Locate every blood parasite and identify its species.
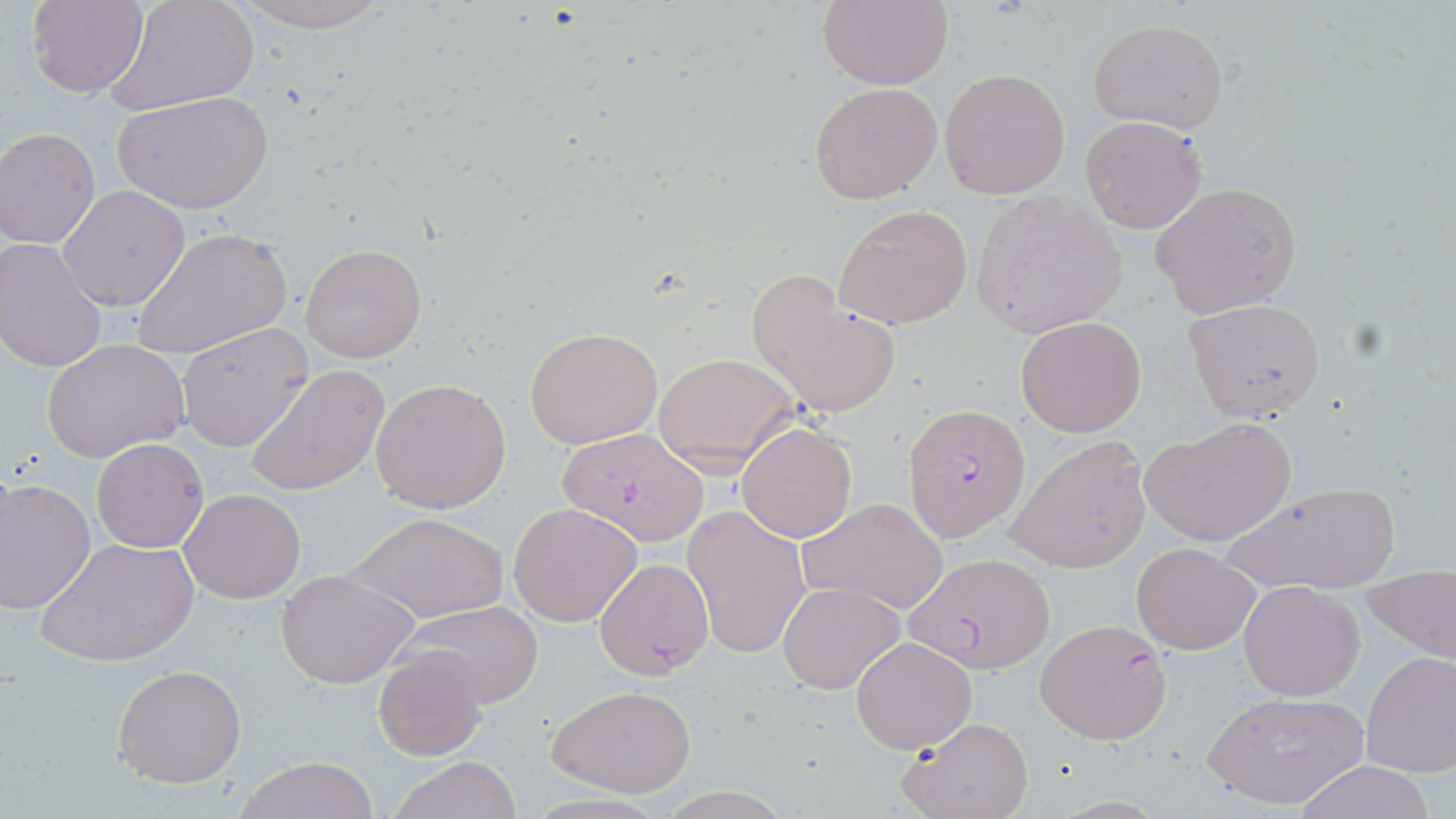
Approximate bounding boxes as named x1/y1/x2/y2 corners in pixels.
Plasmodium falciparum-infected red blood cells: (x1=903, y1=402, x2=1029, y2=540), (x1=558, y1=426, x2=711, y2=546), (x1=904, y1=551, x2=1057, y2=674), (x1=593, y1=557, x2=714, y2=680), (x1=1033, y1=619, x2=1170, y2=745).
No Plasmodium ovale, Plasmodium malariae, Plasmodium vivax, Babesia divergens, or Trypanosoma brucei observed.

Uninfected red blood cell locations: (x1=27, y1=0, x2=147, y2=98), (x1=816, y1=0, x2=952, y2=90), (x1=105, y1=1, x2=259, y2=116), (x1=225, y1=1, x2=397, y2=33), (x1=1087, y1=18, x2=1229, y2=132), (x1=939, y1=66, x2=1072, y2=199), (x1=808, y1=81, x2=943, y2=204), (x1=111, y1=90, x2=274, y2=214), (x1=1080, y1=116, x2=1208, y2=234), (x1=1, y1=128, x2=100, y2=248), (x1=1151, y1=180, x2=1303, y2=320), (x1=56, y1=186, x2=188, y2=312), (x1=971, y1=191, x2=1127, y2=339), (x1=832, y1=202, x2=976, y2=333), (x1=132, y1=226, x2=291, y2=362), (x1=0, y1=238, x2=107, y2=372), (x1=300, y1=243, x2=427, y2=363), (x1=745, y1=269, x2=904, y2=420), (x1=1183, y1=298, x2=1326, y2=422), (x1=1014, y1=315, x2=1148, y2=438), (x1=175, y1=322, x2=314, y2=451), (x1=524, y1=325, x2=662, y2=449), (x1=42, y1=338, x2=190, y2=463), (x1=654, y1=353, x2=803, y2=472), (x1=244, y1=364, x2=390, y2=497), (x1=370, y1=377, x2=512, y2=515), (x1=1140, y1=417, x2=1297, y2=547), (x1=736, y1=420, x2=858, y2=542), (x1=1006, y1=434, x2=1151, y2=572), (x1=91, y1=438, x2=208, y2=552), (x1=1, y1=478, x2=97, y2=615), (x1=1219, y1=479, x2=1401, y2=597), (x1=179, y1=488, x2=305, y2=604), (x1=795, y1=497, x2=950, y2=614), (x1=507, y1=501, x2=644, y2=627), (x1=682, y1=503, x2=811, y2=660), (x1=345, y1=511, x2=509, y2=626), (x1=37, y1=535, x2=197, y2=667), (x1=1131, y1=539, x2=1263, y2=655), (x1=275, y1=568, x2=418, y2=688), (x1=1361, y1=569, x2=1456, y2=668), (x1=1238, y1=581, x2=1365, y2=701), (x1=778, y1=582, x2=905, y2=695), (x1=400, y1=600, x2=545, y2=711), (x1=849, y1=636, x2=978, y2=753), (x1=374, y1=647, x2=489, y2=760), (x1=1361, y1=651, x2=1456, y2=776), (x1=112, y1=663, x2=247, y2=788), (x1=547, y1=684, x2=698, y2=798), (x1=1200, y1=687, x2=1369, y2=811), (x1=899, y1=717, x2=1037, y2=819), (x1=235, y1=755, x2=380, y2=819), (x1=386, y1=755, x2=522, y2=819), (x1=1293, y1=760, x2=1439, y2=819). Slide-level diagnosis: Plasmodium falciparum. Image is 1456×819 pixels. Light microscopy. May-Grünwald-Giemsa-stained preparation. Thin blood smear. Single field of view. 1000x magnification.